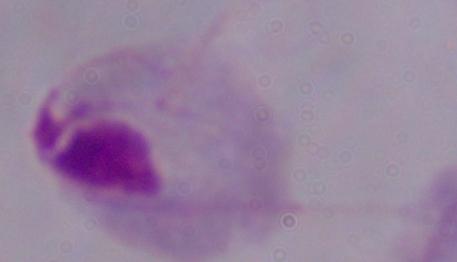

1000x magnification. Photomicrograph. A trichomonad is shown.